State which cell type is depicted.
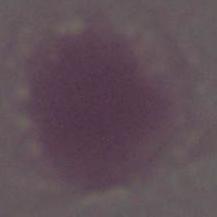

An erythrocyte.

magnification: 1000x
modality: photomicrograph